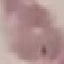 Malaria status: uninfected. Giemsa-stained preparation. Thin smear of blood. Acquired by smartphone through the microscope eyepiece. Automatically extracted cell patch, resized to 64 × 64 pixels.